Name the parasite shown.
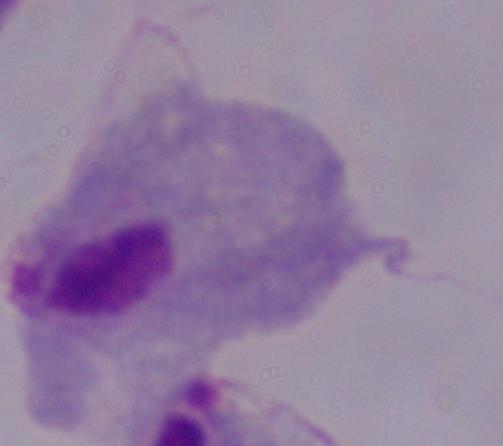

A trichomonad.

{
  "magnification": "1000x",
  "modality": "micrograph"
}